Classify this cell by malaria status.
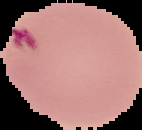
Uninfected.

Segmented cell region on a black background. Image is 142×130 pixels. From a thin blood smear.